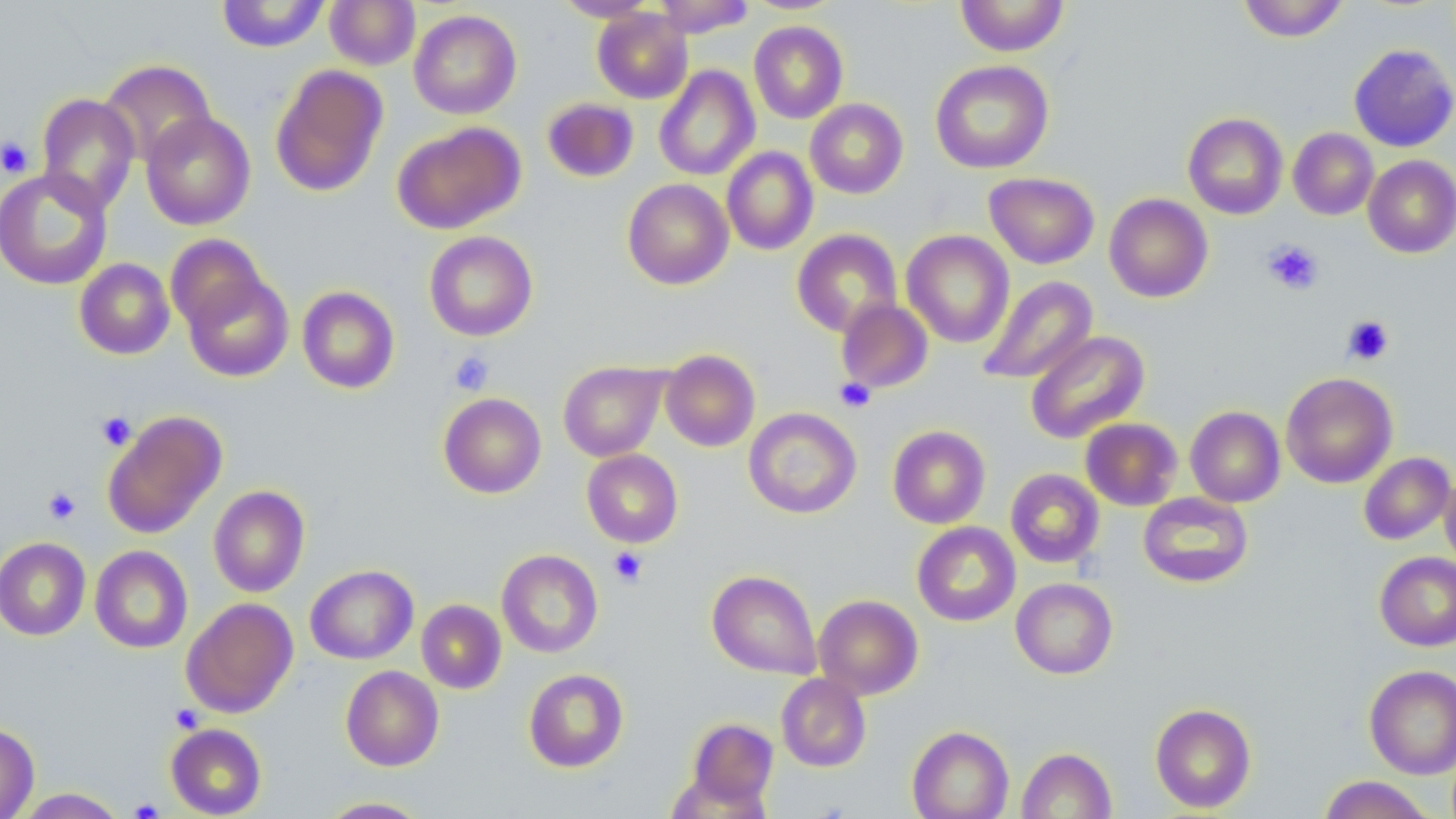
Summary:
  - Coordinate format: approximate bounding boxes as (x1, y1, x2, y2) in pixels
  - Uninfected red blood cell locations: (216, 0, 330, 53), (325, 0, 420, 71), (553, 0, 659, 22), (652, 0, 755, 37), (955, 0, 1070, 56), (1238, 0, 1349, 42), (592, 7, 693, 104), (409, 9, 522, 119), (749, 21, 848, 124), (1349, 44, 1456, 152), (99, 59, 216, 167), (930, 60, 1054, 174), (269, 65, 388, 198), (654, 65, 760, 182), (36, 93, 140, 214), (542, 97, 639, 182), (805, 98, 908, 199), (140, 111, 256, 230), (1183, 113, 1288, 219), (391, 122, 524, 235), (1288, 128, 1379, 220), (722, 147, 818, 255), (1363, 155, 1456, 258), (0, 167, 113, 291), (984, 172, 1099, 269), (622, 178, 733, 290), (1104, 193, 1213, 303), (791, 229, 902, 338), (902, 230, 1014, 348), (424, 231, 537, 341), (165, 234, 268, 332), (74, 258, 175, 360), (182, 270, 294, 382), (977, 275, 1098, 385), (297, 286, 400, 394), (836, 299, 934, 394), (1025, 330, 1150, 444), (660, 349, 760, 452), (558, 361, 667, 461), (1281, 372, 1398, 488), (438, 392, 547, 498), (1185, 406, 1285, 507), (744, 407, 862, 519), (102, 411, 226, 539), (1080, 418, 1182, 511), (887, 425, 991, 528), (582, 449, 683, 547), (1359, 452, 1455, 545), (1005, 468, 1104, 567), (1439, 473, 1456, 575), (208, 485, 310, 597), (1138, 492, 1254, 588), (912, 521, 1021, 627), (0, 537, 91, 640), (90, 545, 193, 653), (496, 549, 603, 657), (1374, 552, 1456, 651), (305, 565, 418, 665), (707, 569, 822, 679), (1011, 577, 1118, 679), (813, 594, 923, 699), (181, 597, 298, 717), (416, 599, 506, 694), (340, 665, 444, 771), (1364, 665, 1456, 779), (523, 668, 629, 772), (776, 673, 871, 772), (1150, 703, 1256, 812), (687, 716, 780, 810), (0, 722, 39, 819), (166, 723, 267, 818), (907, 726, 1013, 819), (1016, 747, 1117, 819), (1317, 776, 1437, 818), (14, 788, 128, 818), (316, 796, 434, 818)
  - Platelet locations: (0, 136, 34, 178), (1262, 239, 1324, 295), (1341, 315, 1394, 365), (448, 351, 494, 395), (835, 378, 875, 413), (95, 411, 136, 450), (43, 486, 81, 524), (608, 546, 648, 587), (170, 704, 205, 733), (129, 798, 164, 818)
  - Slide-level diagnosis: no evidence of blood parasites
  - Modality: light microscopy
  - Preparation: thin blood smear
  - Field of view: single
  - Image size: 1456×819 pixels
  - Stain: May-Grünwald-Giemsa
  - Magnification: 1000x